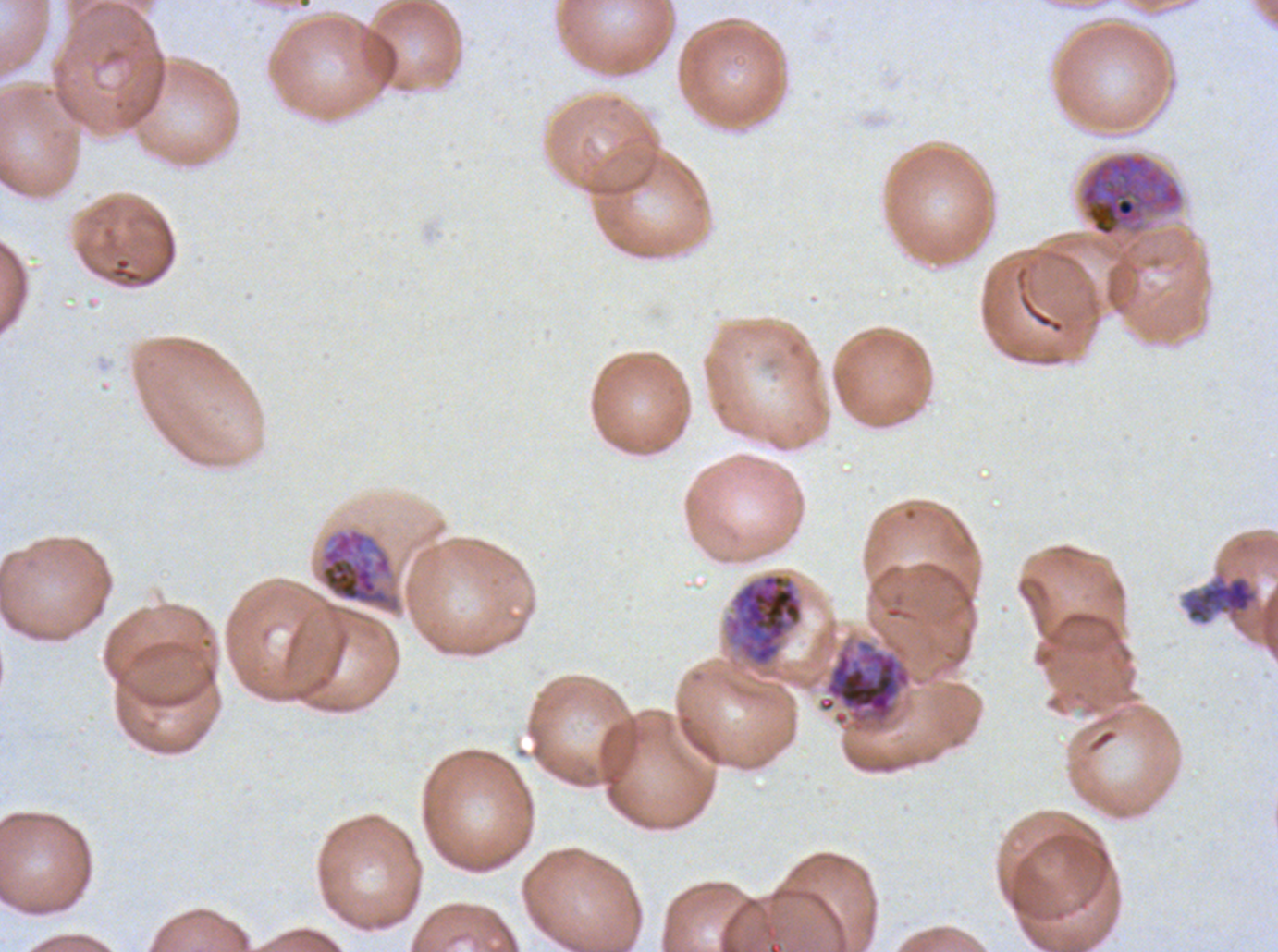 Approximate bounding boxes as {x1, y1, x2, y2} in pixels. Debris locations: {1179, 568, 1260, 627}. Late schizont locations: {319, 528, 400, 612}. Early schizont locations: {1077, 152, 1186, 239}, {726, 572, 804, 667}, {817, 638, 913, 734}. One sub-image of a larger composite. Thin blood smear. Image is 1278×952 pixels. Giemsa-stained preparation. P. falciparum cultured ex vivo for 24 to 48 hours, from a patient in The Gambia. Life-cycle stages observed: early schizont, late schizont.